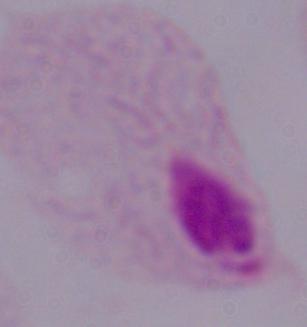

1000x magnification. A trichomonad is shown. Micrograph.